State which parasite is depicted.
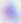
Toxoplasma gondii.

400x magnification. Photomicrograph.